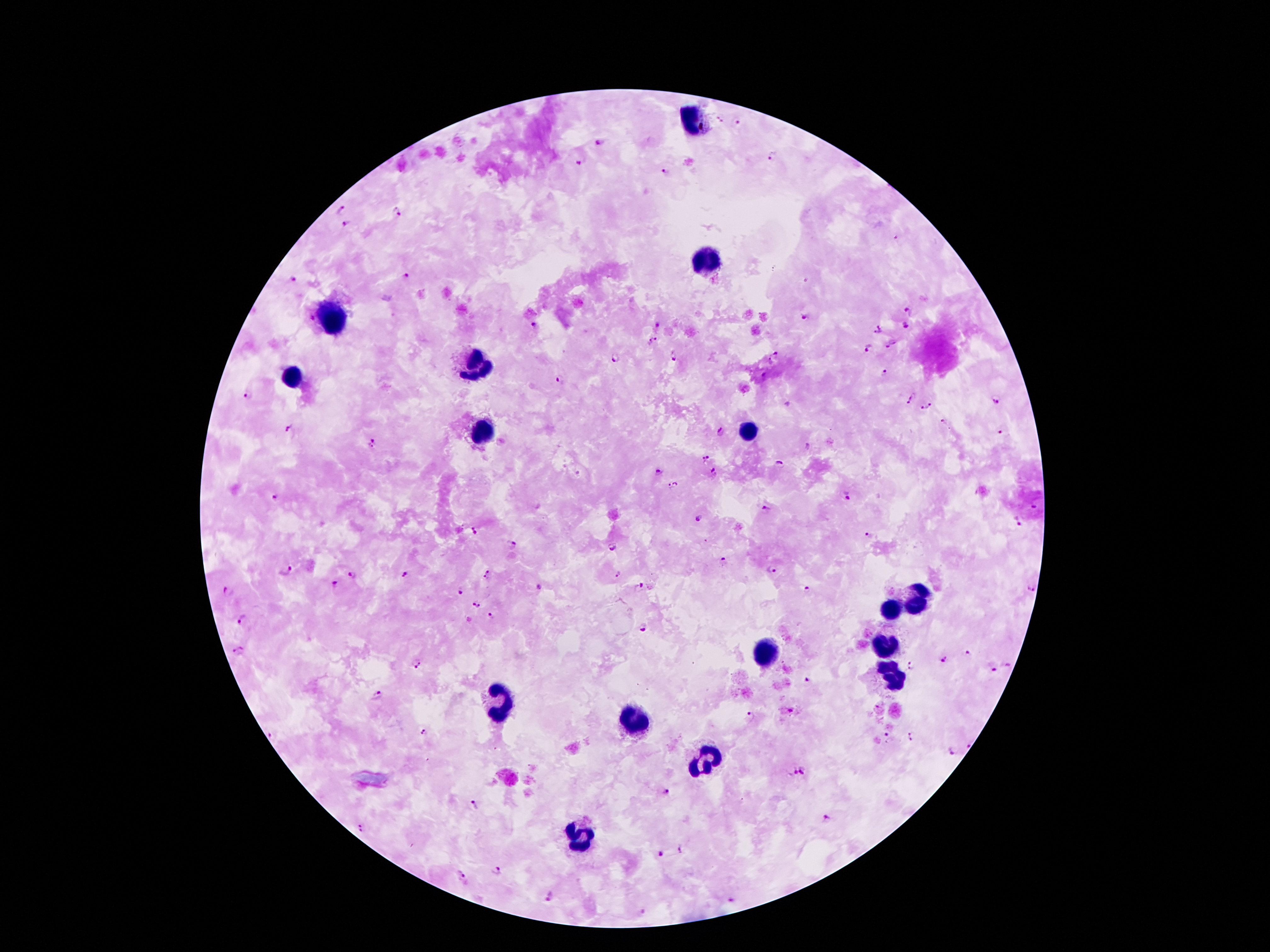 Approximate centers as [x, y] in pixels. Leukocyte locations: [695, 120], [706, 258], [332, 318], [475, 363], [295, 375], [481, 430], [744, 430], [919, 588], [916, 607], [891, 611], [887, 647], [766, 651], [887, 665], [895, 681], [500, 700], [630, 720], [707, 757], [575, 835]. Plasmodium parasite locations: [720, 118], [739, 122], [600, 142], [772, 158], [579, 162], [663, 172], [340, 207], [396, 212], [348, 222], [406, 277], [294, 279], [910, 310], [807, 316], [311, 319], [532, 324], [657, 324], [906, 325], [882, 326], [875, 335], [652, 340], [890, 345], [868, 348], [774, 354], [614, 357], [672, 359], [884, 374], [559, 379], [248, 394], [912, 397], [931, 401], [1000, 402], [906, 406], [924, 408], [943, 422], [290, 429], [1001, 430], [721, 431], [372, 443], [705, 458], [780, 463], [658, 469], [712, 472], [672, 483], [847, 496], [275, 497], [1034, 507], [764, 509], [701, 517], [1018, 521], [476, 530], [868, 535], [512, 545], [613, 547], [722, 561], [285, 568], [771, 570], [487, 573], [615, 573], [353, 575], [406, 575], [335, 583], [641, 585], [540, 586], [806, 590], [230, 591], [461, 591], [1031, 591], [475, 604], [490, 615], [243, 620], [645, 629], [238, 649], [967, 655], [942, 659], [417, 662], [1006, 663], [911, 666], [992, 668], [805, 679], [377, 695], [750, 717], [426, 733], [271, 735], [887, 737], [914, 737], [967, 743], [952, 750], [805, 769], [789, 772], [664, 792], [474, 803], [829, 817], [361, 828], [682, 848], [659, 855], [497, 869], [461, 874], [548, 897], [731, 899]. 100x magnification. Single field of view. Thick blood film. Patient malaria status: positive for Plasmodium falciparum. Image is 1270×952 pixels. Giemsa-stained preparation. Photographed through the microscope eyepiece with a smartphone camera.